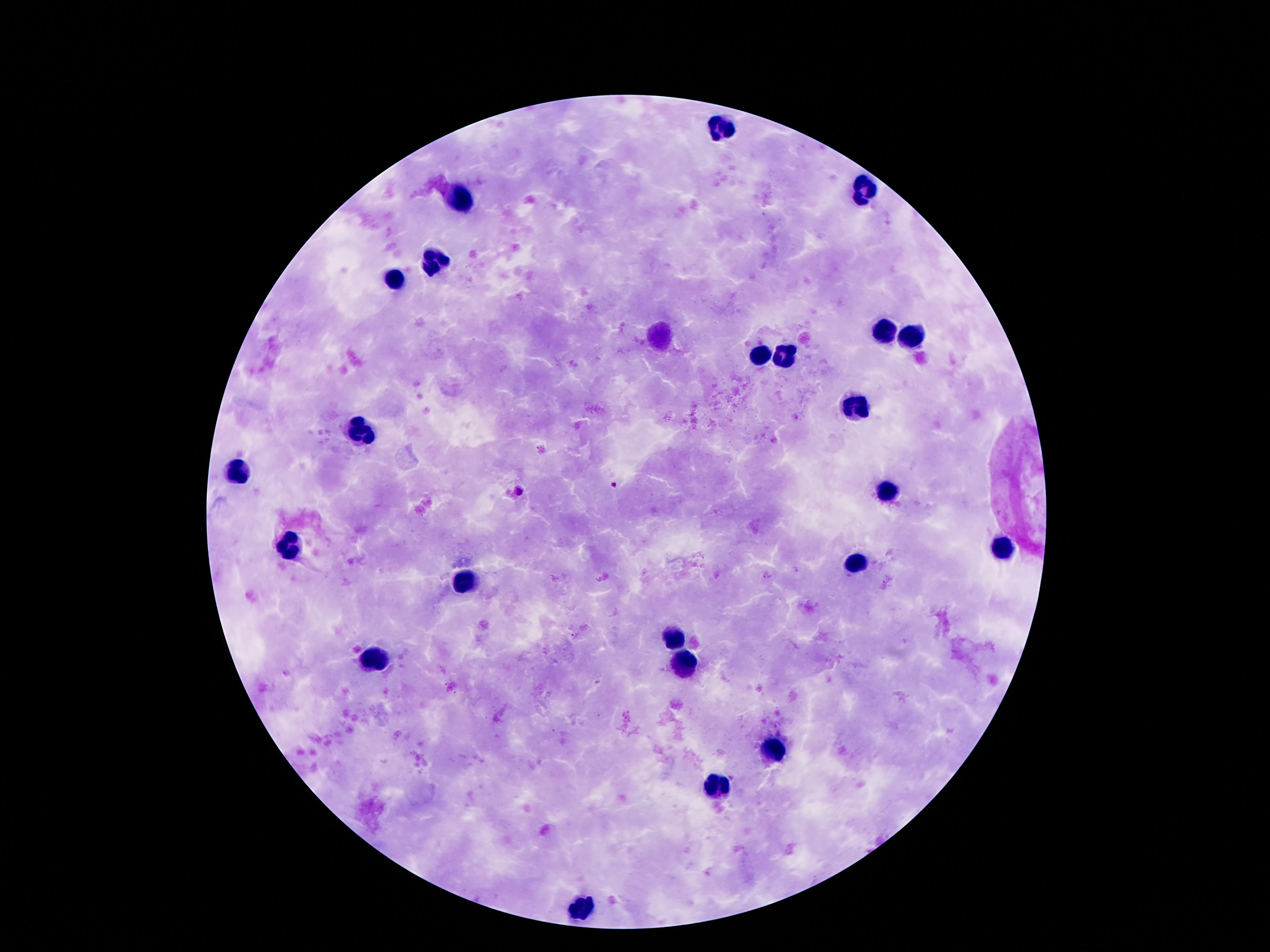
Approximate centers as (x, y) in pixels.
Summary:
  - Leukocyte locations: (719, 130), (863, 190), (459, 197), (432, 264), (391, 277), (885, 330), (916, 334), (760, 352), (787, 353), (855, 404), (363, 434), (238, 472), (887, 494), (1000, 549), (291, 550), (855, 564), (463, 582), (672, 636), (373, 657), (684, 662), (773, 750), (715, 783), (584, 907)
  - Patient malaria status: negative
  - Stain: Giemsa
  - Image size: 1270×952 pixels
  - Preparation: thick peripheral-blood smear
  - Field of view: one from this slide
  - Magnification: 100x
  - Capture: smartphone camera through the microscope eyepiece